Comment on the morphology of the erythrocytes.
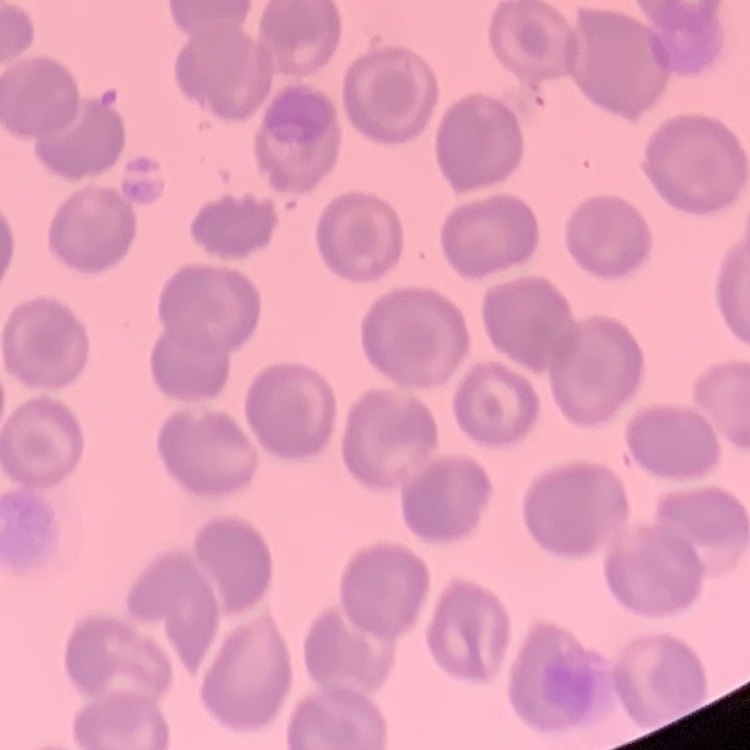
No rouleaux formation.

Summary:
  - Preparation: thin peripheral smear
  - Stain: Field's or Giemsa
  - Image type: one tile cut from a larger photomicrograph